Locate and identify every blood parasite.
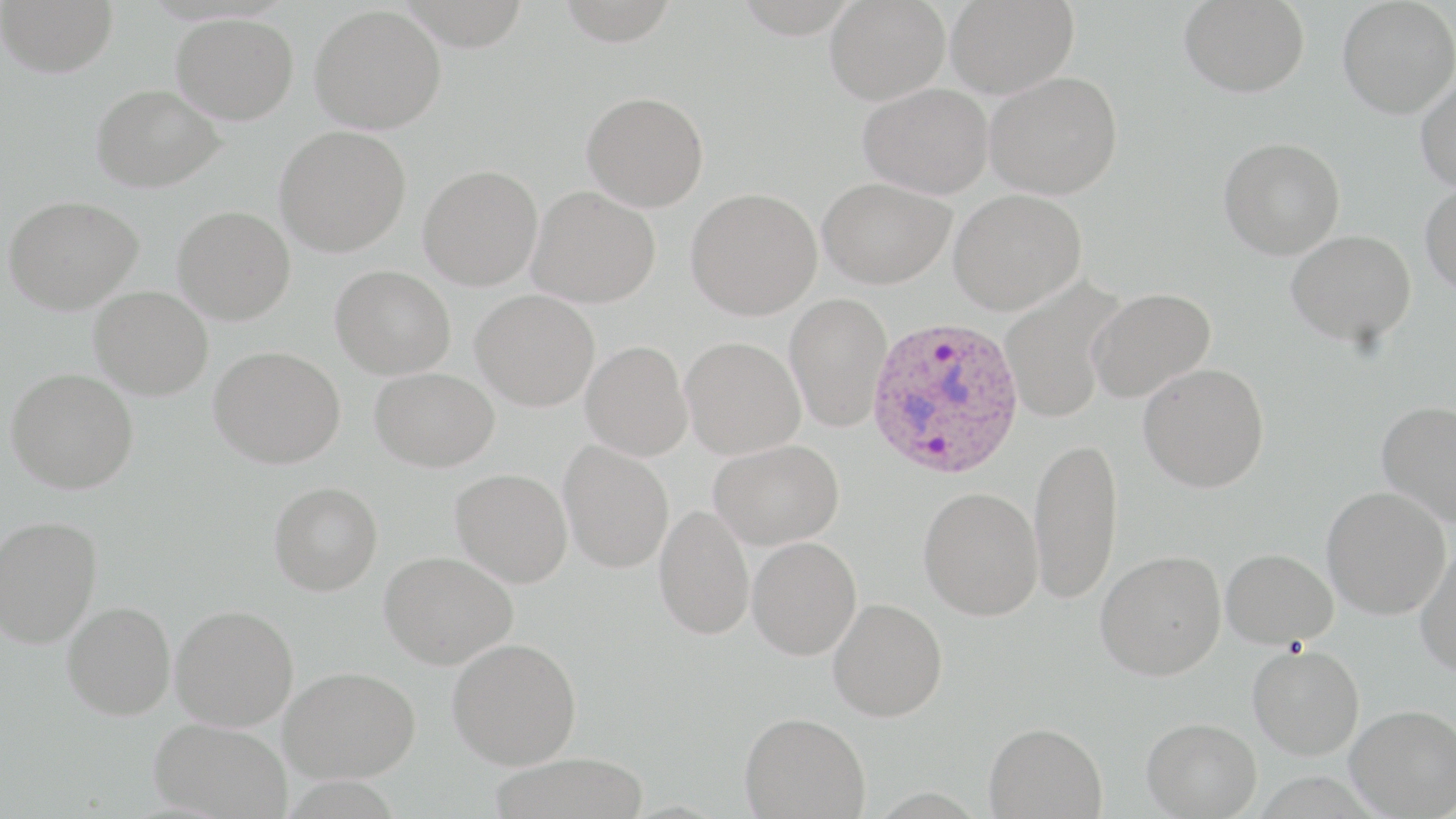

Approximate bounding boxes as named x1/y1/x2/y2 corners in pixels.
Plasmodium ovale-infected red blood cells: (x1=866, y1=315, x2=1024, y2=479).
No Plasmodium falciparum, Plasmodium malariae, Plasmodium vivax, Babesia divergens, or Trypanosoma brucei observed.

Uninfected red blood cell locations: (x1=0, y1=0, x2=118, y2=78), (x1=825, y1=0, x2=949, y2=105), (x1=946, y1=0, x2=1079, y2=98), (x1=1179, y1=0, x2=1309, y2=98), (x1=1337, y1=0, x2=1456, y2=118), (x1=310, y1=5, x2=446, y2=134), (x1=171, y1=13, x2=298, y2=124), (x1=985, y1=71, x2=1123, y2=199), (x1=1415, y1=71, x2=1456, y2=192), (x1=858, y1=83, x2=993, y2=199), (x1=91, y1=84, x2=224, y2=192), (x1=582, y1=91, x2=709, y2=211), (x1=275, y1=125, x2=411, y2=257), (x1=1218, y1=137, x2=1345, y2=259), (x1=418, y1=164, x2=543, y2=291), (x1=818, y1=177, x2=956, y2=288), (x1=1420, y1=182, x2=1456, y2=296), (x1=528, y1=186, x2=661, y2=308), (x1=686, y1=187, x2=823, y2=320), (x1=949, y1=188, x2=1087, y2=314), (x1=4, y1=195, x2=143, y2=314), (x1=173, y1=206, x2=295, y2=325), (x1=1286, y1=230, x2=1416, y2=347), (x1=331, y1=265, x2=456, y2=379), (x1=999, y1=277, x2=1125, y2=422), (x1=89, y1=286, x2=213, y2=400), (x1=1087, y1=287, x2=1216, y2=404), (x1=471, y1=289, x2=600, y2=411), (x1=784, y1=293, x2=893, y2=433), (x1=680, y1=336, x2=805, y2=459), (x1=580, y1=341, x2=693, y2=461), (x1=209, y1=346, x2=346, y2=468), (x1=1138, y1=362, x2=1269, y2=492), (x1=6, y1=367, x2=139, y2=494), (x1=369, y1=367, x2=499, y2=472), (x1=1377, y1=399, x2=1456, y2=526), (x1=1029, y1=436, x2=1123, y2=605), (x1=709, y1=438, x2=844, y2=550), (x1=559, y1=441, x2=674, y2=573), (x1=450, y1=468, x2=572, y2=587), (x1=269, y1=481, x2=383, y2=595), (x1=918, y1=486, x2=1043, y2=620), (x1=1321, y1=486, x2=1451, y2=618), (x1=654, y1=504, x2=754, y2=640), (x1=0, y1=514, x2=102, y2=648), (x1=747, y1=536, x2=861, y2=660), (x1=1415, y1=542, x2=1456, y2=678), (x1=1221, y1=548, x2=1338, y2=648), (x1=380, y1=550, x2=517, y2=669), (x1=1095, y1=551, x2=1226, y2=680), (x1=828, y1=598, x2=947, y2=721), (x1=62, y1=601, x2=176, y2=719), (x1=171, y1=604, x2=298, y2=730), (x1=447, y1=638, x2=582, y2=769), (x1=1247, y1=644, x2=1364, y2=760), (x1=280, y1=666, x2=421, y2=782), (x1=1346, y1=704, x2=1456, y2=817), (x1=740, y1=712, x2=870, y2=818), (x1=149, y1=717, x2=292, y2=819), (x1=1142, y1=717, x2=1262, y2=818), (x1=984, y1=721, x2=1108, y2=818), (x1=488, y1=753, x2=652, y2=818). Slide-level diagnosis: Plasmodium ovale. Optical microscopy. May-Grünwald-Giemsa stain. Captured at 1000x magnification. Image is 1456×819 pixels. One field of a larger specimen. Thin blood film.